Assess the morphology of the red blood cells.
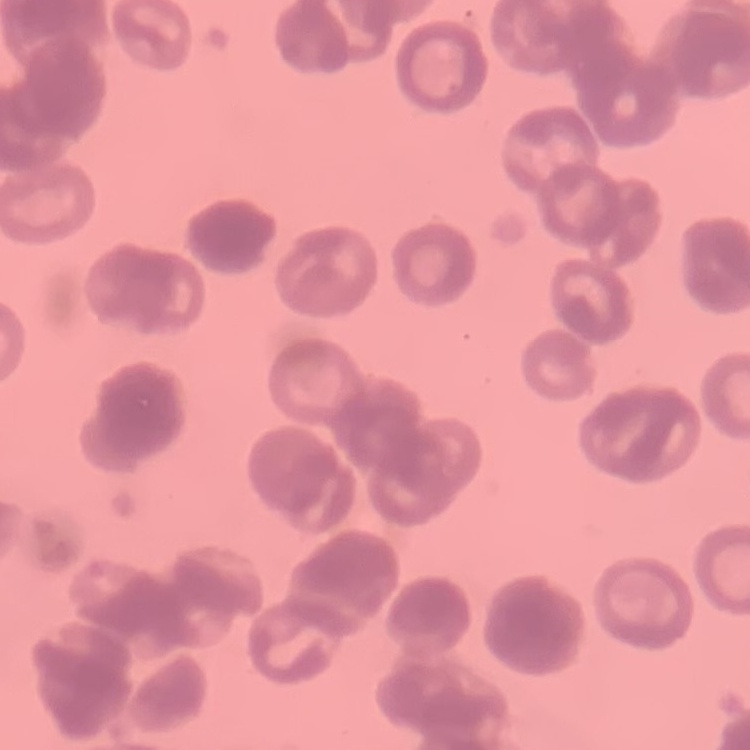
Rouleaux formation.

{
  "preparation": "thin blood film",
  "stain": "Field's or Giemsa",
  "image_type": "one tile cut from a larger photomicrograph"
}